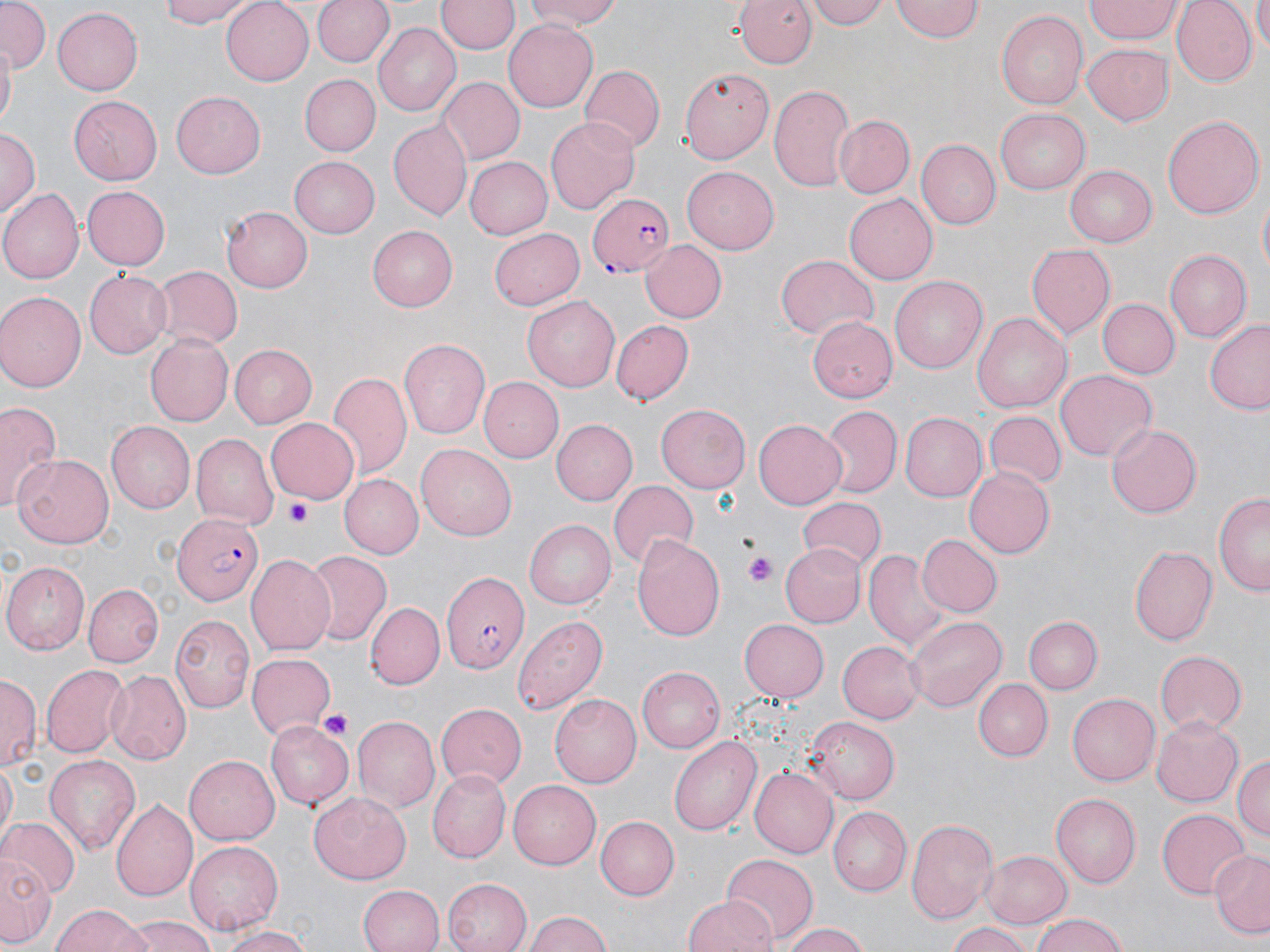
slide_level_diagnosis: Plasmodium falciparum
magnification: 1000x
stain: May-Grünwald-Giemsa
field_of_view: one of a larger specimen
preparation: thin blood film
plasmodium_falciparum_infected_red_blood_cell_locations: 'approximate bounding boxes as [x1, y1, x2, y2] in pixels: [587, 192, 677, 276], [174, 512, 265, 606], [439, 570, 528, 673]'
platelet_locations: 'approximate bounding boxes as [x1, y1, x2, y2] in pixels: [287, 499, 313, 525], [746, 554, 776, 589], [318, 707, 353, 741]'
modality: optical microscopy
uninfected_red_blood_cell_locations: 'approximate bounding boxes as [x1, y1, x2, y2] in pixels: [0, 0, 51, 70], [156, 0, 254, 28], [220, 0, 313, 84], [314, 0, 395, 68], [523, 0, 623, 31], [806, 0, 889, 29], [1085, 0, 1182, 42], [1170, 0, 1256, 86], [1252, 0, 1270, 53], [438, 1, 516, 55], [891, 1, 983, 43], [735, 2, 812, 69], [52, 7, 142, 95], [995, 10, 1089, 111], [504, 21, 598, 113], [373, 24, 462, 116], [1081, 40, 1176, 125], [1, 41, 16, 128], [581, 66, 664, 152], [679, 67, 775, 163], [299, 74, 380, 157], [438, 77, 525, 164], [771, 82, 856, 193], [171, 91, 265, 178], [69, 96, 163, 184], [994, 110, 1089, 193], [1163, 113, 1263, 221], [546, 115, 639, 213], [833, 115, 915, 199], [390, 117, 471, 222], [0, 126, 39, 219], [916, 139, 1000, 230], [291, 155, 380, 238], [466, 156, 554, 239], [681, 165, 782, 254], [1066, 165, 1156, 246], [80, 184, 169, 272], [0, 188, 81, 284], [1256, 191, 1269, 281], [845, 195, 937, 283], [221, 205, 313, 293], [368, 226, 457, 310], [488, 227, 584, 311], [640, 239, 728, 324], [1026, 242, 1116, 338], [1167, 249, 1253, 340], [775, 254, 880, 340], [150, 265, 240, 350], [85, 270, 172, 359], [891, 275, 986, 373], [0, 293, 84, 394], [522, 295, 624, 391], [1099, 298, 1178, 378], [973, 311, 1072, 414], [805, 319, 898, 398], [611, 320, 695, 403], [1205, 320, 1270, 413], [144, 333, 233, 426], [400, 337, 492, 439], [230, 345, 317, 428], [1055, 369, 1155, 461], [330, 370, 412, 481], [477, 376, 563, 464], [0, 399, 64, 513], [656, 403, 751, 492], [823, 406, 901, 495], [899, 411, 986, 502], [983, 412, 1065, 489], [264, 416, 359, 501], [753, 418, 847, 509], [552, 420, 636, 504], [105, 422, 195, 513], [1105, 423, 1199, 518], [191, 433, 278, 529], [417, 443, 516, 537], [13, 454, 114, 548], [963, 467, 1054, 558], [341, 473, 424, 558], [608, 479, 700, 571], [1216, 493, 1269, 597], [796, 498, 885, 571], [524, 519, 618, 609], [632, 533, 725, 641], [917, 533, 1003, 618], [779, 542, 866, 629], [1131, 545, 1219, 646], [864, 549, 949, 649], [303, 551, 391, 647], [245, 554, 337, 657], [2, 562, 88, 653], [84, 583, 162, 666], [368, 601, 444, 691], [170, 613, 255, 713], [513, 613, 609, 716], [905, 615, 1006, 713], [1023, 616, 1100, 694], [738, 619, 828, 702], [837, 639, 922, 724], [1153, 650, 1247, 735], [247, 653, 336, 741], [42, 664, 129, 756], [637, 666, 725, 753], [106, 669, 191, 764], [0, 677, 38, 771], [974, 678, 1052, 762], [1068, 691, 1160, 787], [548, 694, 640, 788], [436, 703, 526, 789], [1151, 715, 1244, 804], [352, 716, 439, 812], [805, 716, 898, 804], [266, 719, 355, 812], [669, 735, 759, 837], [1233, 752, 1270, 844], [183, 754, 278, 846], [43, 755, 141, 857], [1, 761, 16, 844], [751, 768, 837, 857], [426, 770, 510, 863], [508, 780, 601, 870], [308, 793, 408, 883], [1050, 793, 1140, 886], [110, 799, 197, 906], [828, 807, 908, 895], [1155, 808, 1251, 899], [594, 814, 681, 899], [906, 816, 998, 923], [0, 818, 79, 899], [185, 840, 283, 935], [980, 849, 1071, 927], [2, 850, 53, 948], [1208, 850, 1269, 939], [721, 855, 817, 945], [441, 879, 530, 952], [358, 883, 444, 952], [682, 894, 777, 952], [50, 904, 152, 952], [525, 909, 613, 952], [1029, 912, 1131, 952], [124, 917, 219, 952], [776, 921, 873, 951], [947, 921, 1036, 952], [213, 925, 313, 952]'
image_size: 1270×952 pixels